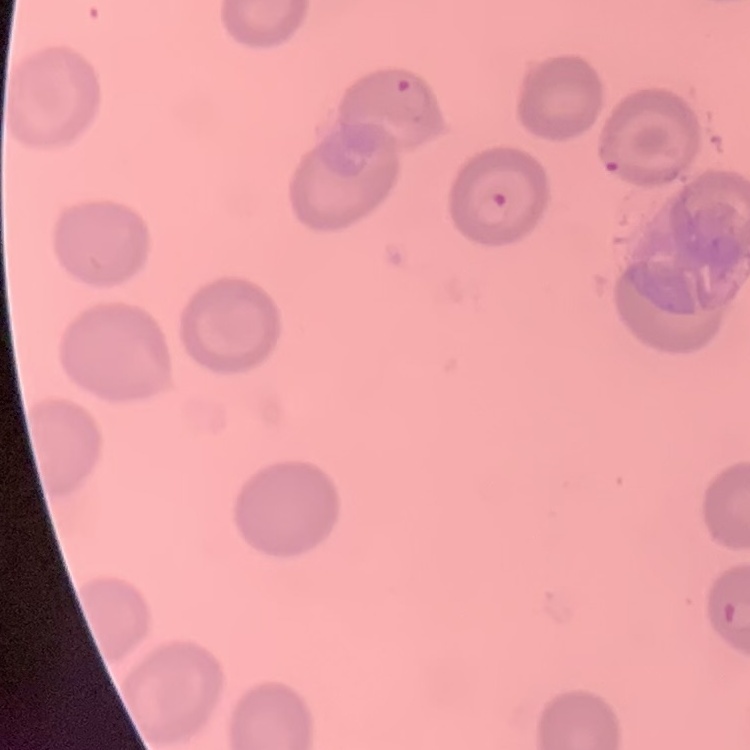

erythrocyte morphology = no rouleaux formation
image type = square crop of a larger photomicrograph
stain = Field's or Giemsa
preparation = thin blood film